Outline each uninfected red blood cell.
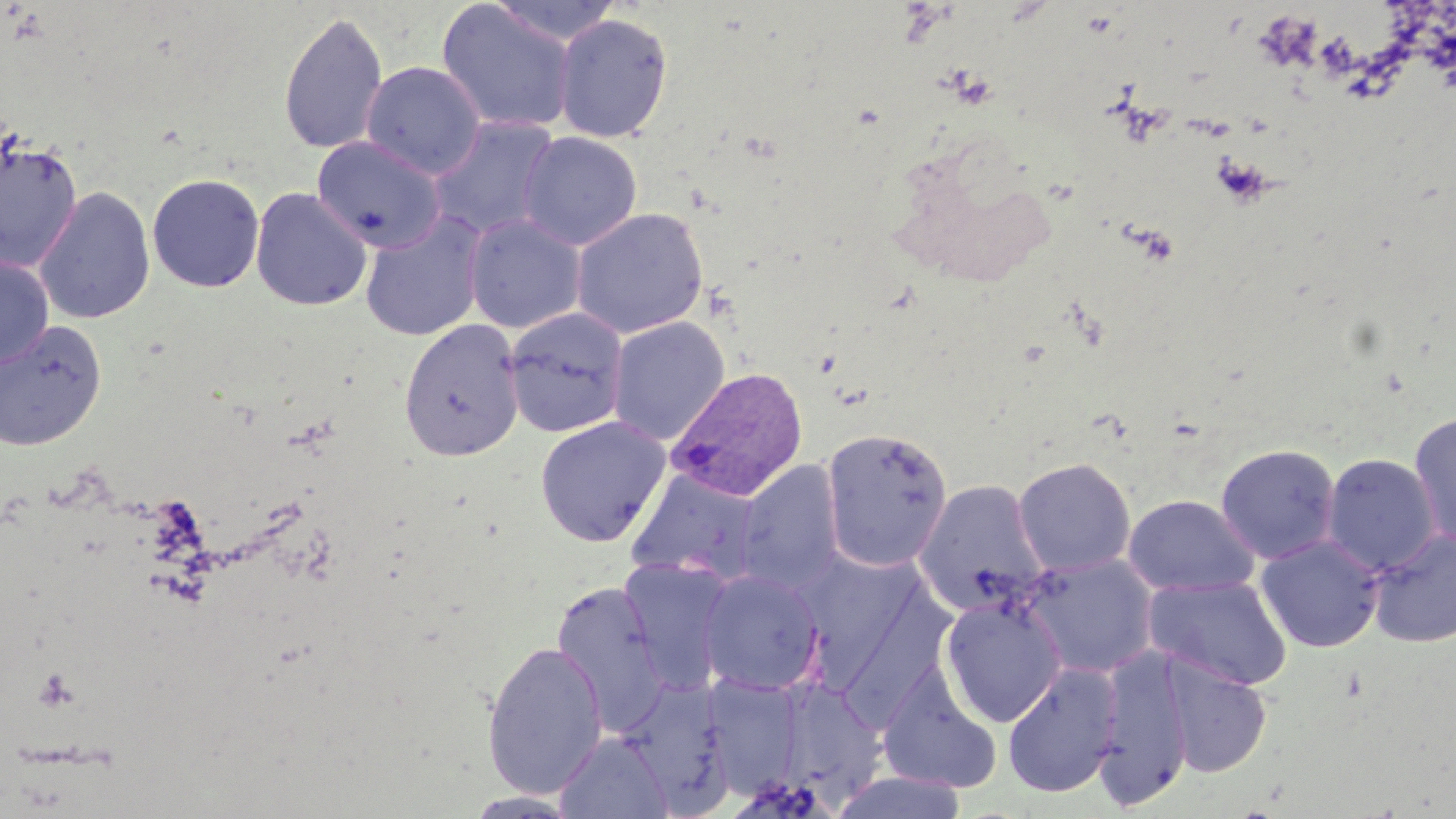

Approximate bounding boxes as (x1, y1, x2, y2) in pixels.
Uninfected red blood cells: (488, 0, 626, 45), (436, 1, 577, 135), (278, 10, 388, 155), (553, 13, 674, 143), (360, 61, 486, 180), (428, 115, 563, 242), (518, 132, 642, 251), (0, 136, 83, 271), (312, 136, 446, 253), (147, 173, 265, 293), (34, 186, 156, 326), (250, 187, 373, 311), (570, 207, 709, 339), (359, 211, 488, 342), (464, 213, 587, 334), (0, 254, 54, 369), (503, 307, 629, 437), (607, 316, 730, 445), (399, 318, 525, 461), (0, 320, 107, 451), (1407, 412, 1456, 551), (534, 415, 672, 546), (820, 427, 953, 572), (1215, 443, 1341, 563), (1321, 452, 1441, 577), (1012, 457, 1137, 576), (734, 460, 845, 594), (625, 469, 764, 588), (913, 478, 1050, 615), (1122, 493, 1261, 597), (1367, 527, 1456, 649), (1256, 534, 1385, 653), (795, 550, 929, 684), (1015, 552, 1160, 679), (617, 557, 737, 691), (698, 570, 825, 696), (1144, 574, 1294, 690), (551, 582, 671, 733), (939, 594, 1068, 727), (482, 639, 608, 799), (1094, 642, 1195, 809), (1158, 652, 1273, 779), (1002, 660, 1122, 799), (876, 664, 1001, 793), (702, 675, 806, 795), (772, 676, 888, 803), (618, 677, 735, 811), (555, 731, 673, 818), (464, 791, 582, 818).

Summary:
  - Plasmodium vivax-infected red blood cell locations: (666, 366, 808, 502)
  - Slide-level diagnosis: Plasmodium vivax
  - Preparation: thin blood smear
  - Modality: optical microscopy
  - Magnification: 1000x
  - Stain: May-Grünwald-Giemsa
  - Image size: 1456×819 pixels
  - Field of view: one of a larger specimen